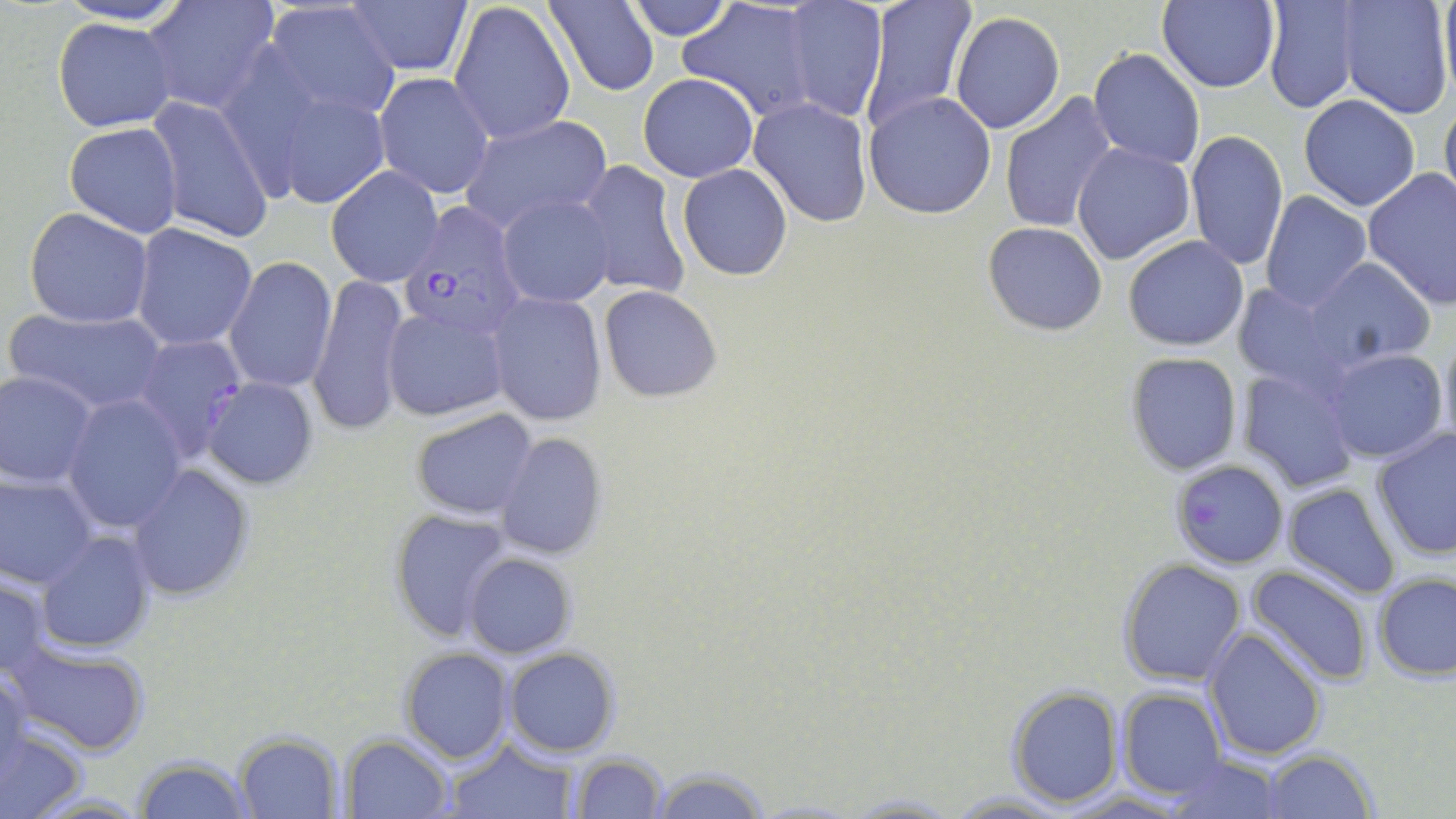

{
  "slide_level_diagnosis": "Plasmodium falciparum",
  "field_of_view": "one of a larger specimen",
  "modality": "light microscopy",
  "image_size": "1456×819 pixels",
  "magnification": "1000x",
  "preparation": "thin blood film",
  "stain": "May-Grünwald-Giemsa",
  "plasmodium_falciparum_infected_red_blood_cell_locations": "approximate bounding boxes as [x1, y1, x2, y2] in pixels: [399, 205, 526, 340], [131, 334, 248, 463], [1170, 458, 1288, 569]",
  "uninfected_red_blood_cell_locations": "approximate bounding boxes as [x1, y1, x2, y2] in pixels: [55, 0, 193, 26], [140, 0, 279, 115], [546, 0, 660, 95], [624, 0, 737, 40], [859, 0, 976, 130], [1262, 0, 1364, 115], [1338, 0, 1454, 121], [344, 1, 471, 77], [1155, 1, 1280, 91], [261, 2, 403, 124], [448, 2, 575, 145], [781, 2, 890, 122], [680, 5, 819, 119], [949, 10, 1065, 135], [53, 16, 178, 133], [1089, 47, 1206, 170], [374, 73, 496, 200], [638, 73, 758, 183], [268, 85, 393, 209], [864, 92, 996, 219], [1000, 93, 1118, 235], [1440, 94, 1456, 218], [1298, 95, 1420, 211], [145, 97, 276, 244], [749, 98, 872, 225], [459, 114, 611, 233], [64, 122, 182, 239], [1184, 130, 1289, 271], [1072, 141, 1196, 266], [576, 160, 690, 301], [678, 164, 792, 280], [327, 166, 444, 286], [1363, 169, 1456, 308], [1260, 191, 1372, 311], [499, 195, 614, 308], [24, 207, 154, 328], [983, 222, 1109, 335], [131, 224, 258, 350], [1123, 235, 1249, 351], [225, 256, 338, 394], [1306, 258, 1434, 364], [309, 276, 410, 434], [1229, 282, 1347, 389], [598, 285, 722, 403], [487, 293, 606, 426], [3, 307, 168, 416], [383, 308, 510, 422], [1437, 328, 1456, 452], [1321, 347, 1448, 464], [1125, 351, 1243, 476], [1240, 368, 1360, 493], [0, 370, 98, 489], [201, 377, 320, 490], [63, 395, 188, 532], [409, 409, 539, 520], [1371, 427, 1456, 560], [494, 432, 607, 561], [128, 463, 256, 602], [0, 472, 98, 591], [1282, 482, 1402, 599], [387, 508, 512, 641], [36, 529, 157, 654], [463, 554, 576, 657], [1118, 557, 1248, 686], [1246, 563, 1375, 686], [0, 572, 53, 679], [1374, 573, 1456, 679], [1202, 628, 1327, 761], [5, 640, 153, 756], [503, 646, 620, 756], [400, 647, 513, 763], [0, 666, 32, 785], [1005, 684, 1124, 807], [1117, 687, 1227, 799], [0, 721, 87, 818], [234, 732, 342, 817], [343, 734, 453, 817], [443, 738, 579, 819], [1262, 747, 1376, 818], [569, 752, 669, 819], [1163, 755, 1284, 818], [133, 758, 257, 818], [647, 765, 771, 819], [943, 790, 1081, 817], [21, 791, 152, 818], [836, 794, 966, 818]"
}